State which parasite is depicted.
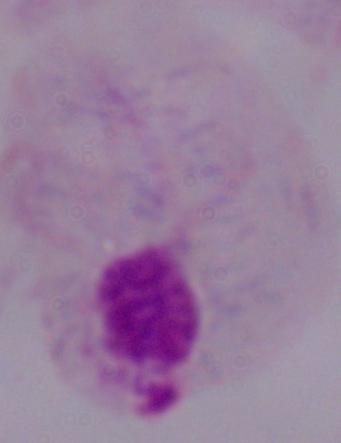

A trichomonad.

1000x magnification. Photomicrograph.